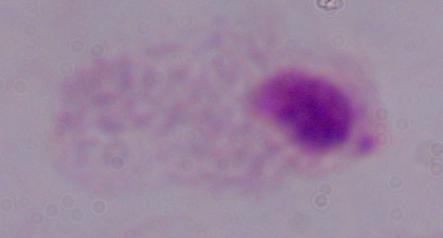

1000x magnification. A trichomonad is seen. Micrograph.